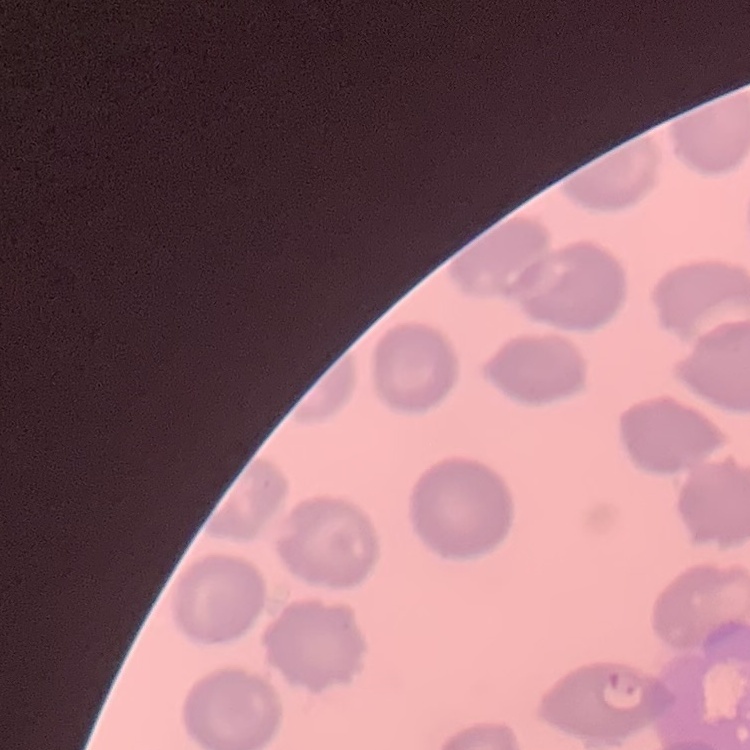

Summary:
  - Red blood cell morphology: no rouleaux formation
  - Image type: square crop of a larger photomicrograph
  - Stain: Field's or Giemsa
  - Preparation: thin blood film